Identify the blood parasite species.
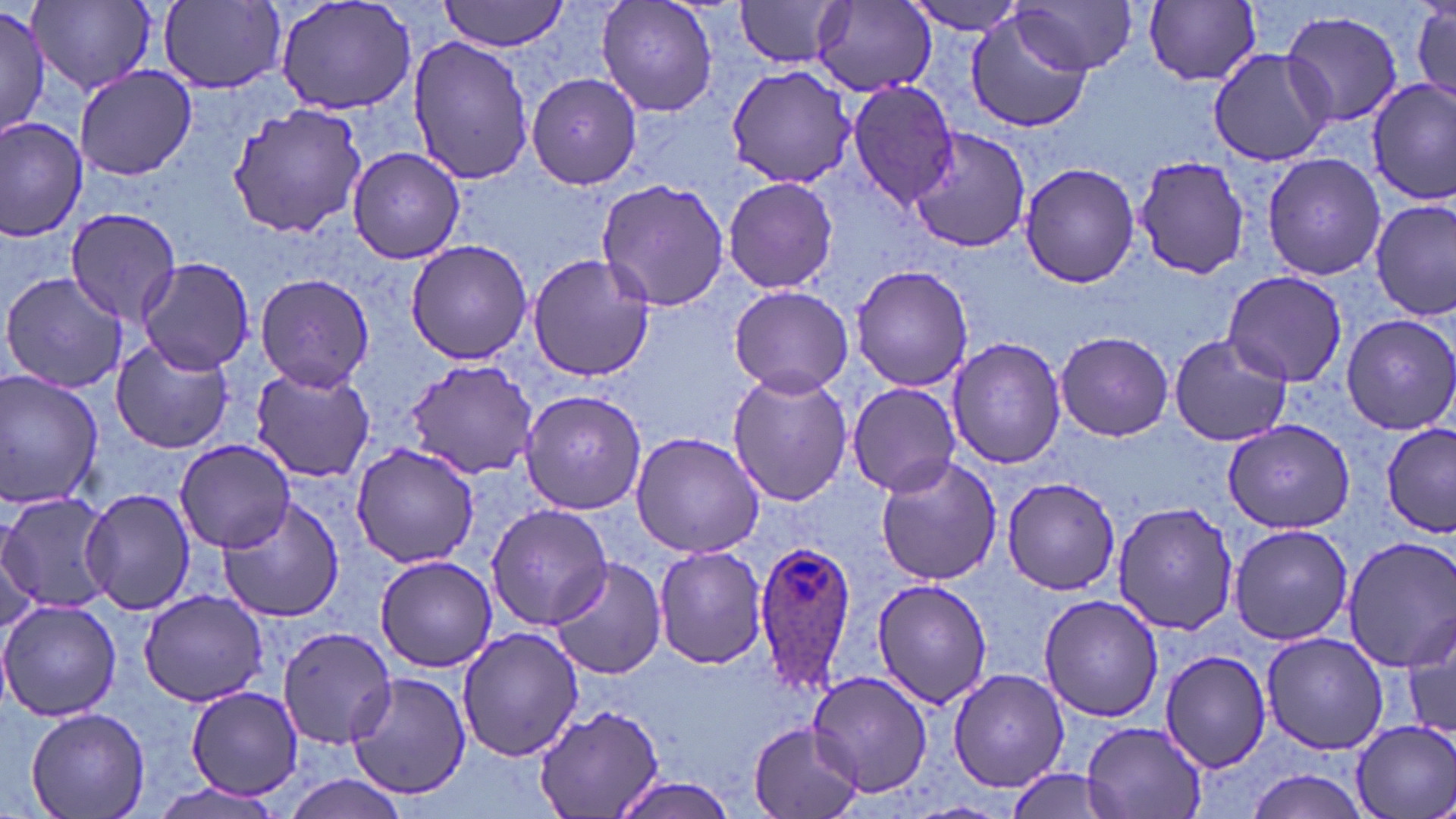

Plasmodium ovale.

Summary:
  - Coordinate format: approximate bounding boxes as [x1, y1, x2, y2] in pixels
  - Plasmodium ovale-infected red blood cell locations: [755, 539, 863, 697]
  - Uninfected red blood cell locations: [275, 0, 418, 114], [440, 0, 569, 52], [594, 0, 721, 119], [733, 0, 850, 69], [902, 0, 1033, 35], [1411, 0, 1456, 111], [30, 1, 156, 95], [1015, 1, 1139, 76], [159, 2, 288, 93], [1139, 2, 1265, 89], [809, 3, 935, 95], [0, 4, 48, 136], [963, 9, 1095, 133], [1281, 11, 1405, 129], [406, 36, 533, 184], [1209, 47, 1333, 166], [74, 66, 197, 180], [726, 66, 855, 187], [525, 72, 645, 190], [845, 80, 957, 209], [1369, 81, 1456, 203], [227, 101, 371, 239], [0, 118, 88, 241], [908, 123, 1030, 255], [346, 146, 466, 264], [1262, 154, 1387, 281], [1136, 155, 1255, 278], [1018, 163, 1140, 286], [721, 174, 840, 294], [594, 177, 733, 312], [1372, 200, 1454, 320], [66, 207, 182, 323], [405, 239, 533, 365], [524, 251, 657, 382], [136, 256, 257, 373], [851, 265, 975, 392], [1220, 269, 1350, 386], [1, 271, 126, 392], [254, 273, 375, 391], [729, 285, 853, 397], [1342, 313, 1456, 434], [1055, 330, 1174, 442], [1168, 333, 1292, 448], [946, 335, 1066, 469], [110, 338, 233, 455], [404, 357, 539, 480], [248, 364, 375, 484], [725, 368, 853, 507], [0, 372, 103, 508], [845, 381, 961, 497], [519, 389, 648, 516], [1222, 417, 1356, 533], [1378, 425, 1456, 534], [630, 431, 766, 558], [175, 438, 298, 552], [350, 442, 480, 569], [874, 455, 1001, 588], [1000, 476, 1122, 597], [79, 486, 197, 615], [0, 491, 114, 613], [217, 496, 345, 625], [1111, 501, 1241, 636], [486, 503, 614, 628], [1228, 523, 1354, 646], [1338, 534, 1455, 674], [653, 545, 768, 670], [374, 555, 499, 673], [546, 556, 668, 680], [871, 576, 993, 711], [139, 589, 267, 707], [1038, 594, 1165, 721], [0, 600, 121, 722], [1404, 611, 1456, 745], [278, 625, 400, 749], [454, 626, 584, 763], [1260, 630, 1388, 755], [1159, 648, 1271, 773], [948, 668, 1068, 790], [804, 669, 934, 797], [348, 673, 474, 799], [184, 687, 302, 801], [535, 702, 665, 818], [23, 707, 150, 819], [1348, 717, 1456, 819], [1081, 720, 1208, 819], [748, 721, 863, 819], [1239, 767, 1378, 818], [1002, 769, 1121, 817], [607, 774, 743, 819], [147, 779, 287, 819]
  - Modality: optical microscopy
  - Stain: May-Grünwald-Giemsa
  - Preparation: thin blood film
  - Magnification: 1000x
  - Field of view: single
  - Image size: 1456×819 pixels